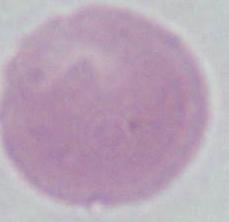
modality = micrograph
magnification = 1000x
identification = erythrocyte